Locate every Plasmodium parasite.
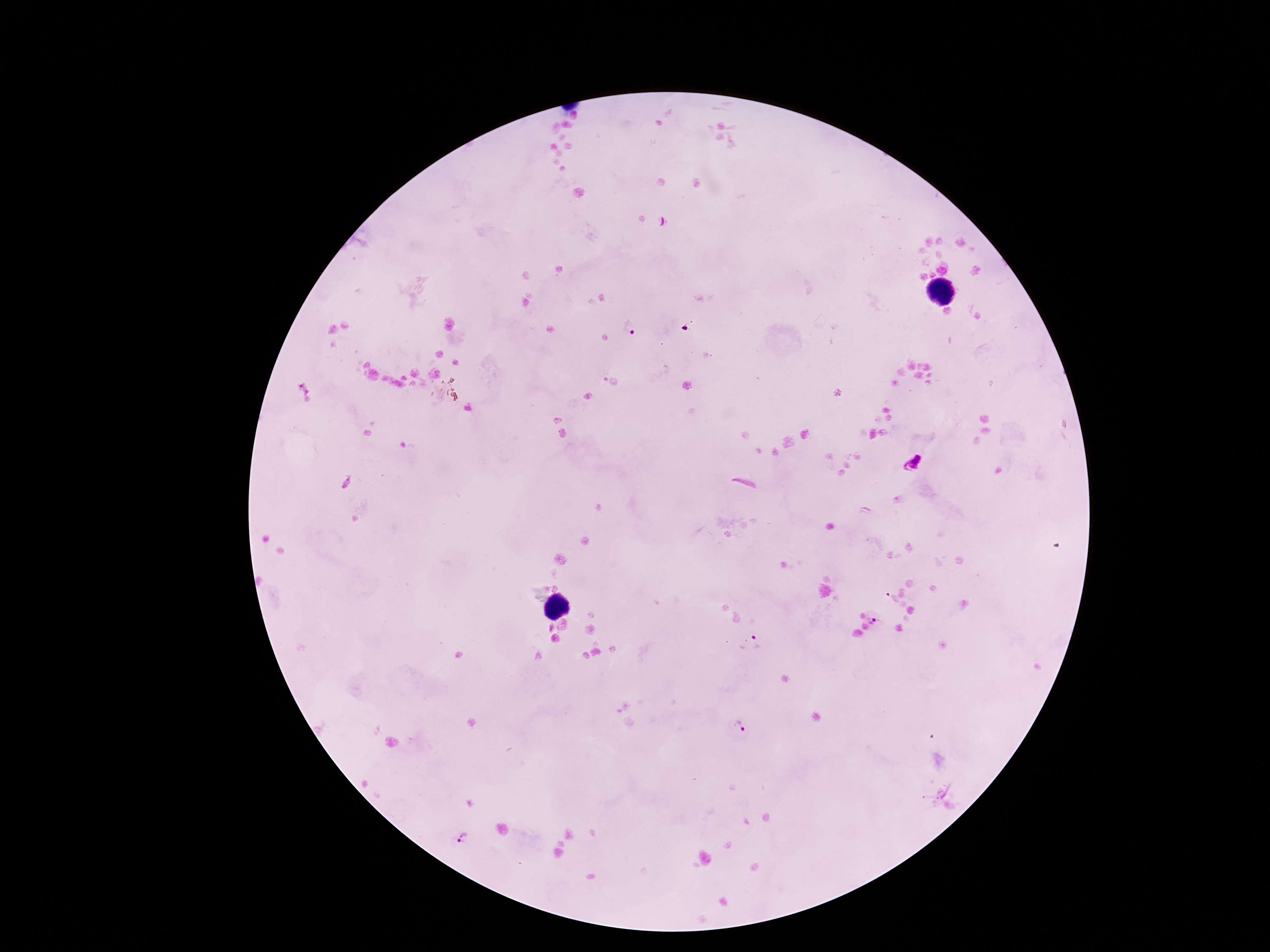
Approximate centers as (x, y) in pixels.
Plasmodium parasites: (627, 328), (912, 463), (874, 620), (750, 643), (739, 727), (465, 837).

Giemsa-stained preparation. Patient malaria status: infected. Photographed through the microscope eyepiece with a smartphone camera. Thick blood smear. Image is 1270×952 pixels. 100x magnification. Single field of view.